Point out each Plasmodium parasite.
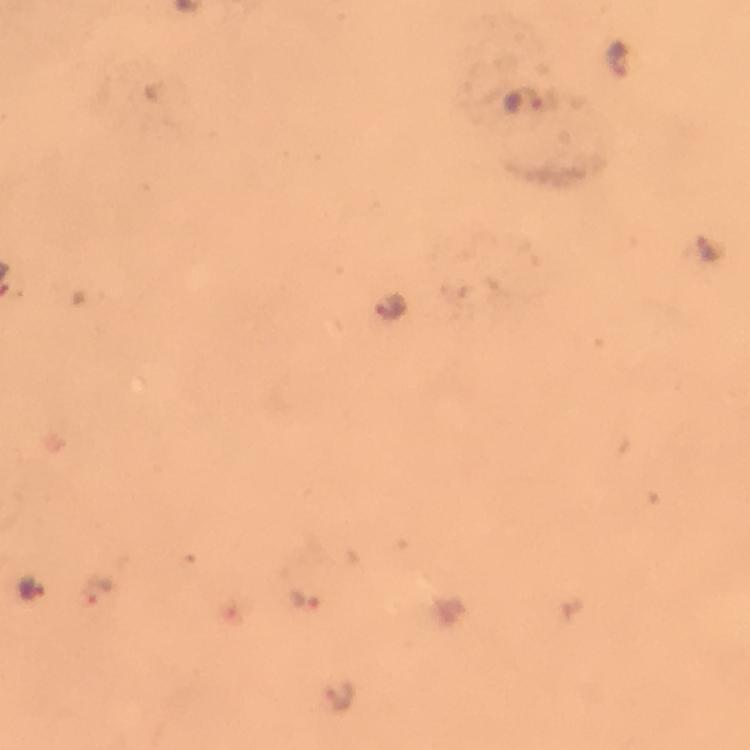
Approximate object centers, in pixels from the top-left corner.
Plasmodium parasites: (x=620, y=54), (x=705, y=248), (x=389, y=308), (x=34, y=590), (x=97, y=591), (x=305, y=598), (x=339, y=694).

magnification = 100x
immersion oil = used
cropped from = a single field of view
preparation = thick smear
context = from a malaria diagnostic workup
image size = 750×750 pixels
capture = smartphone mounted on the microscope
stain = Giemsa